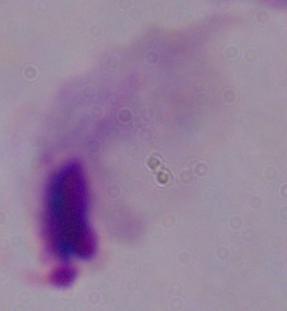

{
  "modality": "micrograph",
  "magnification": "1000x",
  "identification": "trichomonad"
}